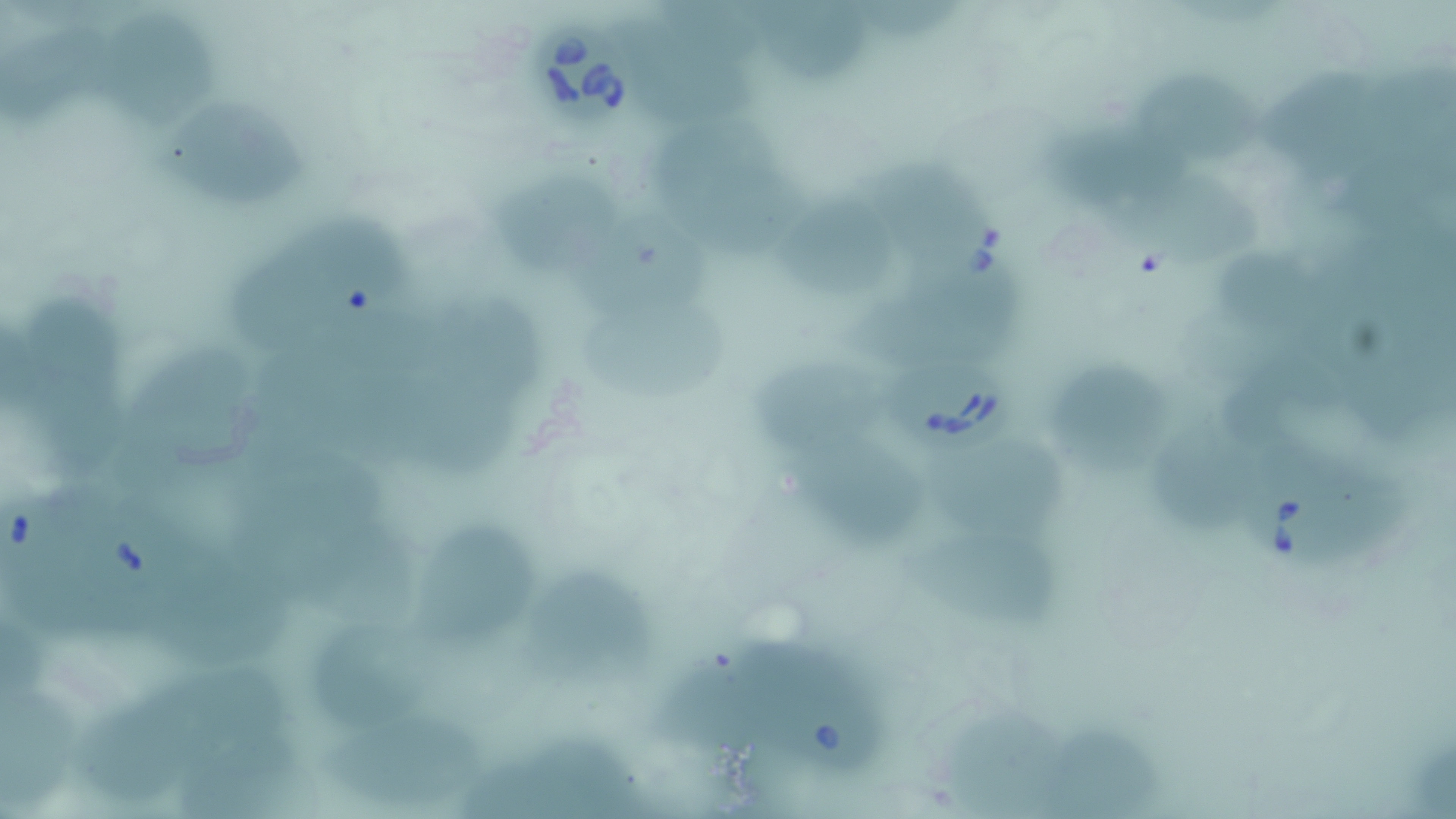

{
  "slide_level_diagnosis": "Babesia divergens",
  "stain": "May-Grünwald-Giemsa",
  "uninfected_red_blood_cell_locations": "approximate bounding boxes as (x1, y1, x2, y2) in pixels: (768, 5, 890, 85), (871, 5, 961, 46), (5, 18, 114, 135), (634, 21, 774, 120), (113, 26, 217, 120), (1263, 65, 1366, 163), (1145, 77, 1276, 175), (157, 96, 310, 203), (1043, 127, 1185, 204), (668, 131, 814, 249), (1123, 173, 1260, 271), (496, 175, 619, 271), (772, 196, 905, 294), (589, 208, 706, 313), (292, 214, 428, 308), (232, 247, 322, 322), (1227, 258, 1325, 330), (433, 289, 555, 368), (29, 290, 133, 373), (853, 291, 1014, 367), (594, 310, 737, 401), (134, 338, 245, 463), (265, 344, 366, 451), (753, 348, 875, 442), (1047, 357, 1182, 471), (19, 369, 129, 475), (418, 384, 532, 469), (1158, 415, 1240, 529), (944, 447, 1074, 538), (227, 459, 381, 549), (804, 459, 934, 541), (420, 513, 542, 641), (918, 546, 1077, 633), (181, 572, 304, 671), (536, 572, 666, 674), (326, 611, 449, 722), (643, 650, 755, 739), (3, 676, 114, 806), (76, 694, 177, 796), (941, 706, 1043, 814), (334, 722, 505, 809), (1050, 726, 1166, 810), (185, 727, 343, 819)",
  "magnification": "1000x",
  "modality": "light microscopy",
  "field_of_view": "single",
  "image_size": "1456×819 pixels",
  "preparation": "thin blood smear",
  "babesia_divergens_infected_red_blood_cell_locations": "approximate bounding boxes as (x1, y1, x2, y2) in pixels: (531, 29, 641, 129), (865, 159, 1014, 282), (879, 358, 1019, 459), (1235, 450, 1414, 576), (761, 659, 877, 780)"
}